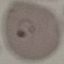

{
  "malaria_status": "parasitized",
  "capture": "smartphone through the microscope eyepiece",
  "stain": "Giemsa",
  "preparation": "thin blood smear",
  "image_type": "cell patch, automatically extracted from a larger field of view and resized to 64 × 64 pixels"
}